Report the malaria status of this cell.
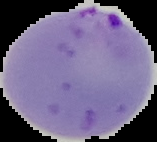

It is parasitized.

image_size: 157×142 pixels
image_type: segmented cell region on a black background
preparation: thin blood film